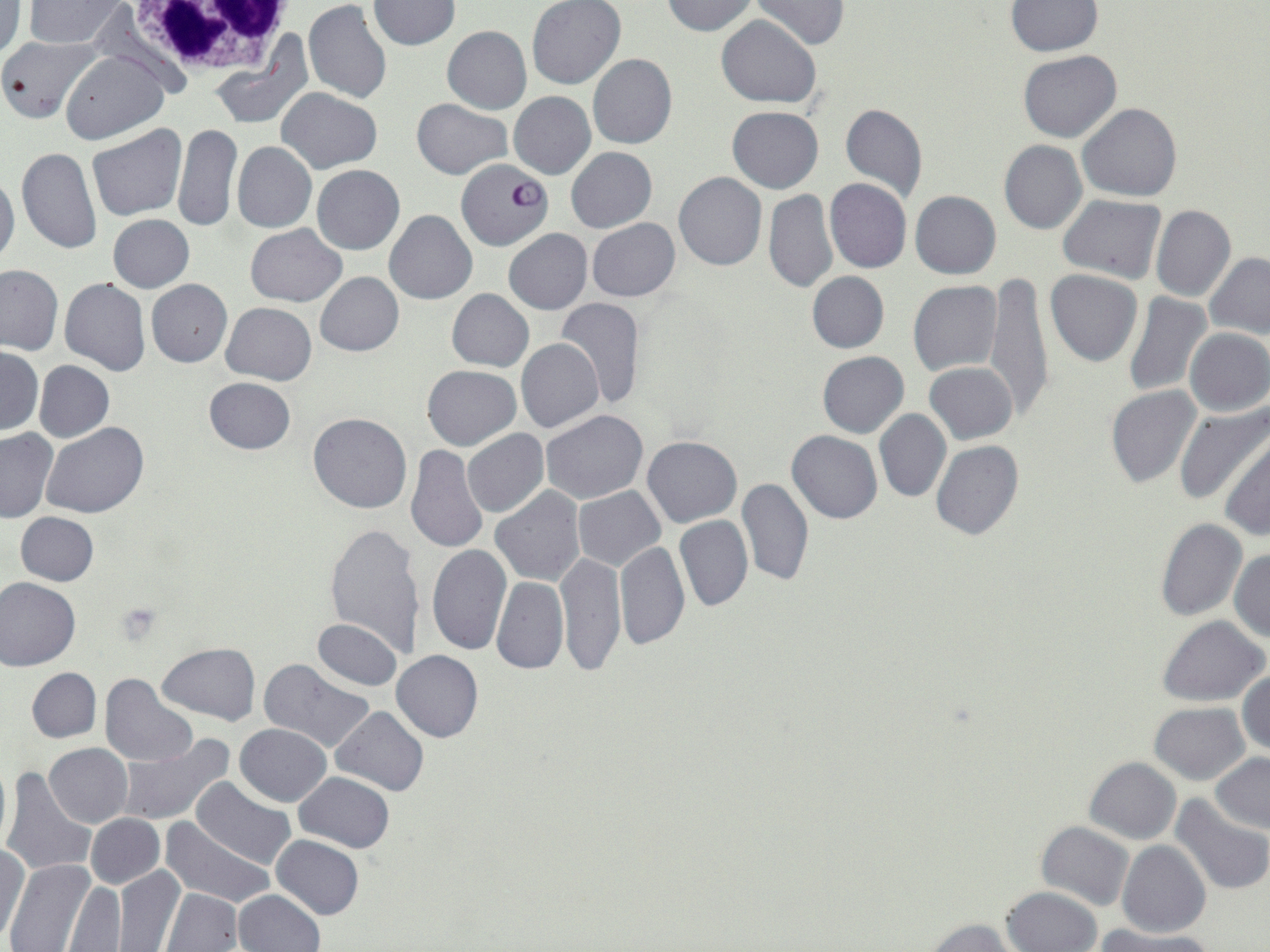

{
  "slide_level_diagnosis": "Plasmodium falciparum",
  "image_size": "1270×952 pixels",
  "preparation": "thin blood film",
  "white_blood_cell_locations": "approximate bounding boxes as [x1, y1, x2, y2] in pixels: [117, 0, 299, 82]",
  "modality": "optical microscopy",
  "stain": "May-Grünwald-Giemsa",
  "plasmodium_falciparum_infected_red_blood_cell_locations": "approximate bounding boxes as [x1, y1, x2, y2] in pixels: [456, 160, 552, 252]",
  "uninfected_red_blood_cell_locations": "approximate bounding boxes as [x1, y1, x2, y2] in pixels: [23, 0, 127, 47], [369, 0, 459, 50], [528, 0, 625, 89], [662, 0, 760, 36], [302, 1, 391, 103], [751, 1, 850, 50], [1006, 1, 1100, 55], [0, 3, 26, 62], [716, 15, 822, 107], [442, 26, 532, 114], [0, 37, 103, 124], [0, 37, 97, 124], [1019, 51, 1121, 142], [61, 52, 167, 144], [588, 54, 677, 149], [276, 88, 381, 173], [509, 92, 595, 179], [412, 99, 512, 179], [840, 103, 928, 203], [1077, 103, 1183, 202], [727, 106, 824, 192], [172, 123, 241, 232], [87, 125, 188, 220], [999, 140, 1086, 234], [232, 142, 316, 233], [16, 146, 101, 254], [565, 147, 656, 232], [312, 166, 404, 254], [0, 171, 20, 270], [673, 172, 767, 272], [824, 179, 912, 274], [764, 191, 837, 294], [910, 191, 1001, 278], [1058, 195, 1166, 284], [1151, 205, 1236, 302], [385, 210, 477, 304], [107, 215, 194, 293], [587, 218, 680, 301], [245, 225, 347, 306], [503, 229, 593, 314], [1204, 252, 1270, 339], [0, 264, 63, 355], [1045, 269, 1143, 366], [806, 271, 889, 353], [315, 272, 403, 356], [984, 274, 1053, 419], [59, 277, 150, 376], [146, 279, 233, 367], [909, 282, 1001, 376], [145, 289, 313, 374], [447, 289, 534, 372], [1122, 292, 1211, 397], [554, 297, 645, 409], [221, 302, 317, 384], [1184, 327, 1269, 416], [516, 338, 604, 432], [0, 348, 42, 434], [816, 351, 909, 438], [35, 361, 113, 441], [925, 362, 1018, 444], [422, 365, 521, 450], [203, 378, 296, 455], [1106, 385, 1200, 488], [1176, 404, 1269, 507], [541, 409, 648, 503], [874, 409, 952, 504], [308, 413, 412, 514], [40, 423, 148, 519], [0, 428, 56, 522], [463, 429, 548, 518], [787, 431, 882, 523], [1220, 434, 1269, 541], [643, 436, 742, 526], [931, 440, 1024, 540], [406, 444, 488, 555], [735, 476, 813, 587], [490, 486, 586, 587], [574, 486, 666, 570], [16, 512, 99, 585], [674, 514, 753, 611], [1155, 518, 1247, 621], [324, 524, 426, 661], [616, 541, 690, 651], [426, 544, 511, 654], [1228, 548, 1270, 642], [556, 550, 626, 676], [491, 575, 568, 674], [0, 577, 81, 670], [1157, 616, 1269, 706], [313, 619, 402, 691], [157, 643, 260, 726], [392, 650, 483, 742], [259, 658, 374, 753], [27, 667, 101, 742], [1237, 668, 1270, 757], [101, 674, 197, 765], [1149, 702, 1250, 784], [331, 705, 428, 796], [235, 723, 332, 806], [117, 734, 233, 826], [44, 743, 132, 827], [1210, 754, 1269, 832], [0, 757, 11, 855], [1084, 757, 1181, 844], [3, 767, 94, 878], [295, 772, 394, 852], [191, 777, 296, 868], [1169, 795, 1270, 896], [85, 814, 164, 889], [159, 818, 275, 909], [1036, 821, 1135, 911], [272, 835, 364, 920], [1117, 840, 1211, 939], [1, 843, 30, 944], [5, 857, 98, 952], [113, 865, 185, 952], [66, 881, 125, 950], [1002, 885, 1103, 952], [160, 888, 242, 952], [232, 890, 325, 952], [923, 917, 1020, 952], [1095, 926, 1214, 952]",
  "platelet_locations": "approximate bounding boxes as [x1, y1, x2, y2] in pixels: [114, 601, 161, 645]",
  "magnification": "1000x",
  "field_of_view": "one of a larger specimen"
}